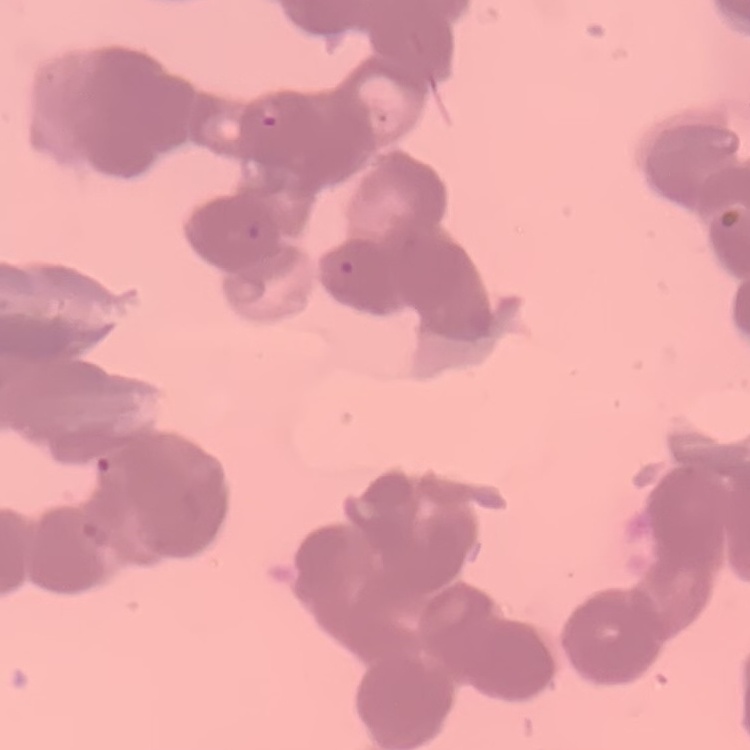 The red blood cells exhibit rouleaux formation. Thin peripheral smear. Stained with either Field's or Giemsa. One tile cut from a larger photomicrograph.